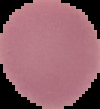
Cell region segmented out of the field of view; the surrounding area is masked to black. Malaria status: uninfected. From a thin blood smear. Image is 100×109 pixels.